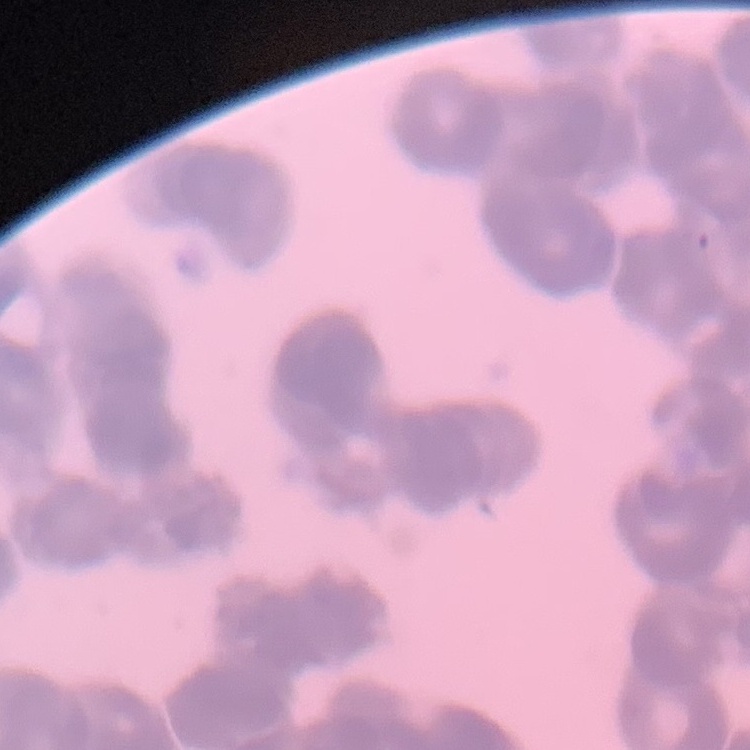
Summary:
  - Erythrocyte morphology: rouleaux formation
  - Image type: one tile cut from a larger photomicrograph
  - Stain: Field's or Giemsa
  - Preparation: thin blood film